Evaluate for malaria.
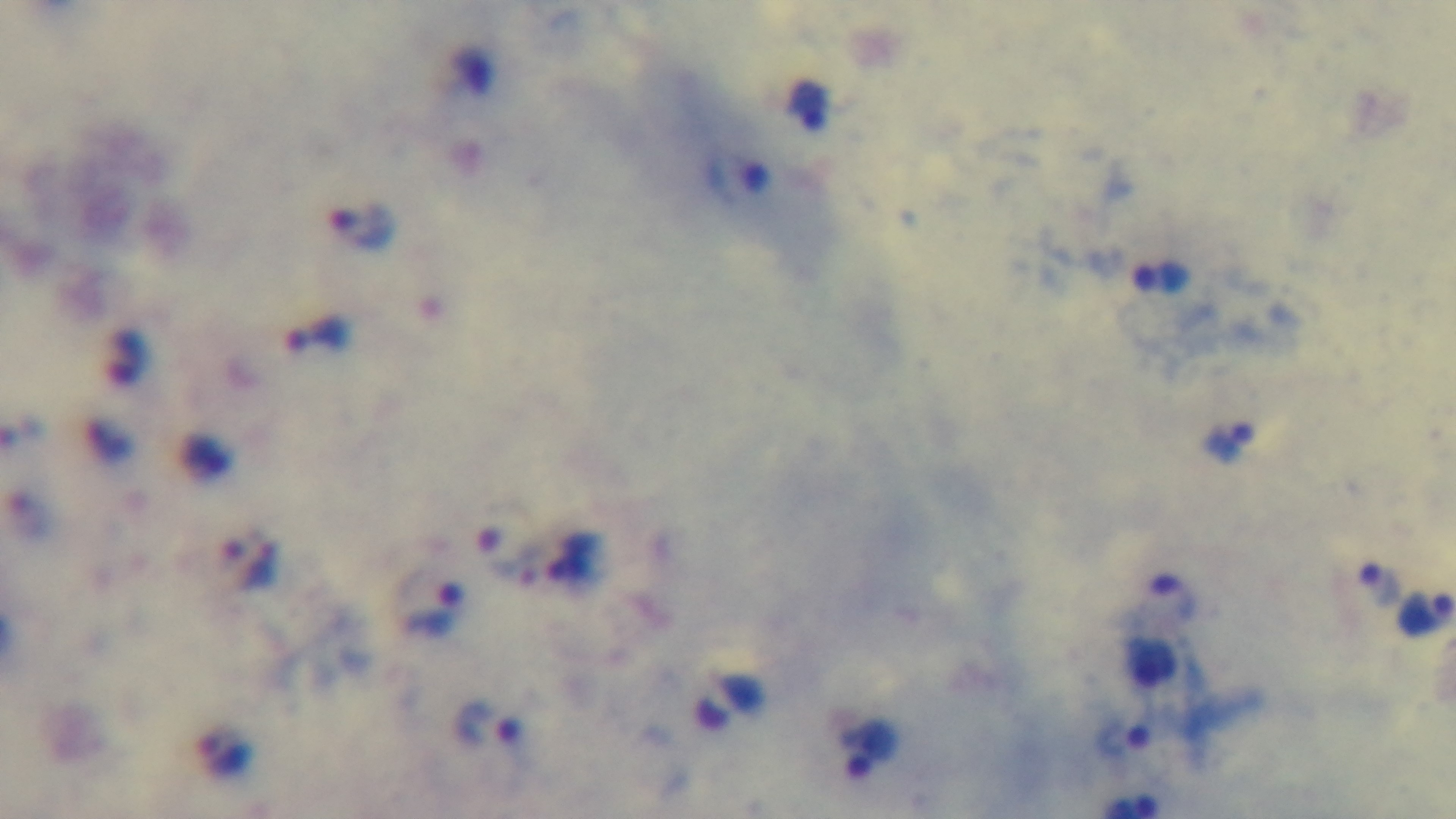
Infected.

modality = light microscopy
field of view = single
preparation = thick
capture = mounted 4K digital camera
objective = 100x oil immersion
stain = Giemsa